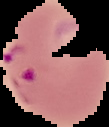

Summary:
  - Image type: cell region segmented out of the field of view; surrounding area masked to black
  - Image size: 109×127 pixels
  - Preparation: thin blood smear
  - Malaria status: parasitized